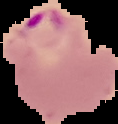 Image is 118×124 pixels. From a thin blood smear. Cell region segmented out of the field of view; the surrounding area is masked to black. Result: Plasmodium parasites identified.